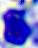

400x magnification. Micrograph. A white blood cell is seen.